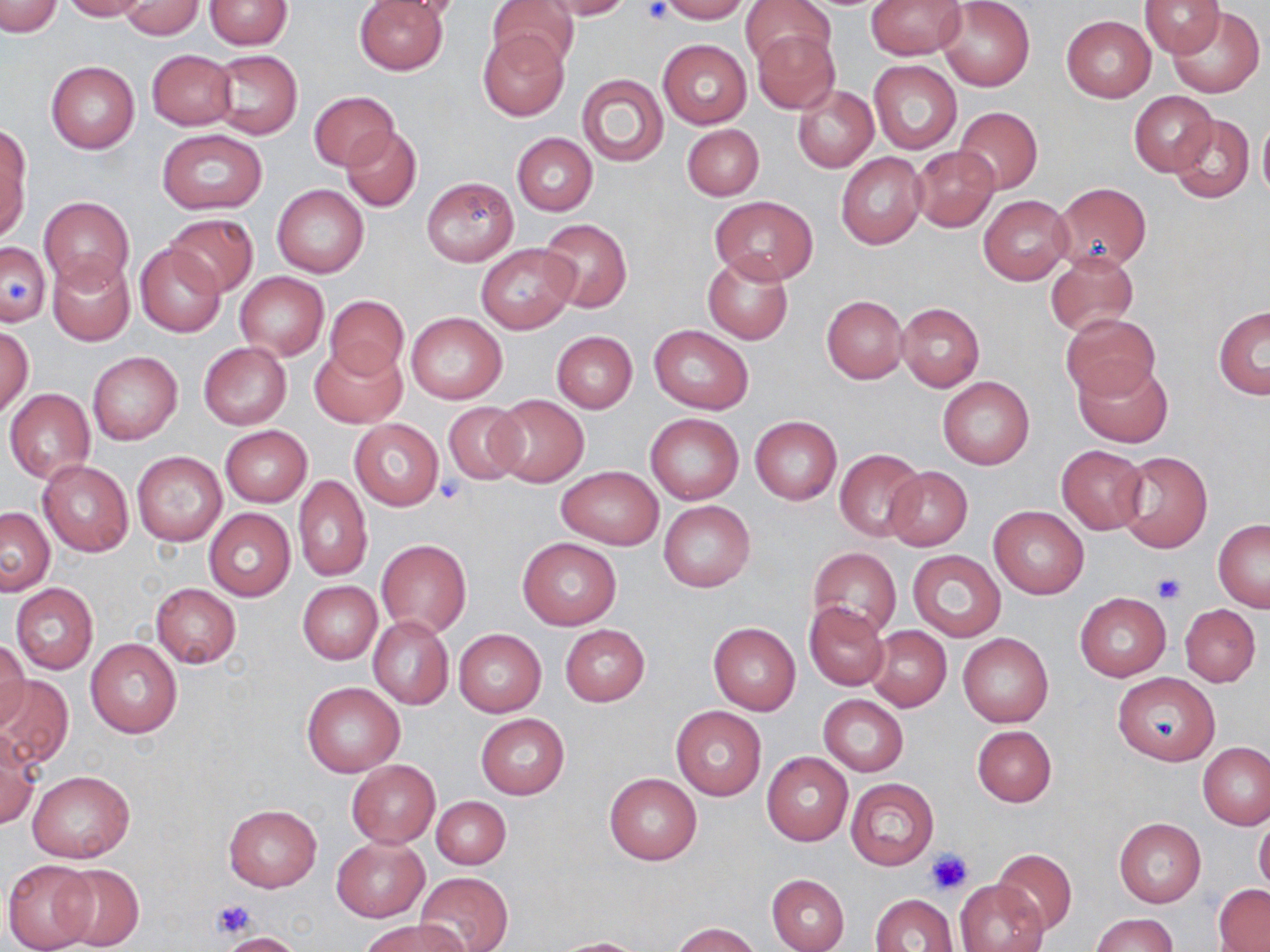
Approximate bounding boxes as [x1, y1, x2, y2] in pixels. Platelet locations: [637, 1, 671, 25], [7, 277, 33, 306], [434, 476, 465, 501], [1152, 573, 1187, 604], [927, 848, 974, 894], [211, 898, 253, 938]. Uninfected red blood cell locations: [1, 0, 61, 38], [60, 0, 150, 21], [204, 0, 292, 49], [353, 0, 447, 75], [377, 0, 469, 22], [487, 0, 579, 75], [541, 0, 632, 20], [659, 0, 749, 22], [741, 0, 835, 69], [866, 0, 962, 58], [1139, 0, 1226, 57], [937, 1, 1035, 90], [117, 2, 205, 39], [1166, 4, 1265, 98], [1060, 15, 1155, 102], [478, 30, 568, 120], [751, 30, 840, 114], [658, 39, 751, 127], [146, 49, 238, 131], [209, 49, 303, 139], [46, 60, 139, 153], [869, 60, 962, 155], [576, 73, 669, 167], [792, 85, 877, 172], [1129, 90, 1218, 175], [309, 91, 397, 171], [954, 106, 1042, 195], [1169, 114, 1254, 203], [1258, 115, 1270, 203], [682, 124, 764, 200], [339, 126, 422, 213], [0, 127, 30, 240], [156, 128, 267, 214], [512, 133, 598, 215], [911, 148, 999, 231], [836, 152, 927, 250], [421, 177, 518, 266], [1054, 182, 1151, 271], [272, 184, 369, 278], [38, 195, 134, 292], [978, 195, 1073, 284], [710, 196, 817, 283], [163, 214, 258, 297], [539, 218, 632, 312], [1, 239, 51, 328], [135, 242, 226, 337], [475, 244, 578, 332], [702, 251, 793, 345], [1044, 251, 1138, 338], [48, 255, 135, 347], [236, 272, 327, 358], [821, 294, 908, 383], [324, 295, 407, 381], [896, 303, 986, 391], [1213, 306, 1269, 399], [407, 312, 506, 404], [1061, 312, 1160, 402], [1, 325, 33, 418], [649, 325, 753, 414], [551, 331, 637, 413], [198, 342, 291, 429], [309, 344, 405, 427], [87, 351, 182, 445], [1074, 359, 1172, 447], [937, 376, 1035, 470], [5, 389, 96, 483], [488, 395, 589, 487], [442, 402, 526, 483], [646, 413, 743, 504], [749, 416, 841, 504], [349, 419, 443, 510], [219, 425, 312, 506], [1056, 445, 1147, 534], [833, 448, 925, 541], [131, 451, 227, 546], [1117, 451, 1213, 553], [39, 461, 134, 557], [883, 466, 972, 550], [556, 467, 664, 549], [292, 475, 373, 581], [658, 500, 756, 592], [988, 506, 1090, 599], [1, 507, 54, 595], [204, 509, 296, 601], [1213, 518, 1270, 611], [517, 537, 622, 629], [377, 539, 471, 638], [808, 547, 901, 639], [907, 550, 1006, 642], [298, 580, 382, 664], [10, 583, 98, 674], [151, 583, 241, 668], [1075, 593, 1171, 680], [804, 602, 890, 691], [1179, 604, 1262, 686], [368, 616, 454, 709], [708, 622, 801, 716], [866, 624, 951, 711], [560, 625, 649, 706], [454, 629, 546, 716], [958, 633, 1053, 728], [84, 638, 182, 737], [0, 640, 30, 729], [1114, 673, 1222, 765], [0, 674, 75, 770], [302, 682, 404, 776], [818, 694, 908, 777], [671, 706, 766, 800], [475, 713, 570, 799], [971, 725, 1056, 806], [0, 732, 39, 828], [1197, 743, 1270, 831], [761, 751, 854, 846], [347, 760, 440, 848], [29, 771, 134, 863], [605, 773, 701, 865], [846, 778, 939, 870], [433, 795, 511, 870], [224, 804, 321, 892], [1255, 817, 1270, 895], [1114, 818, 1206, 907], [330, 836, 428, 921], [994, 849, 1077, 934], [2, 858, 98, 952], [55, 863, 143, 951], [415, 871, 513, 952], [766, 874, 849, 952], [956, 879, 1048, 952], [1214, 886, 1270, 951], [871, 893, 958, 952], [1089, 913, 1179, 952], [361, 919, 466, 952], [672, 922, 762, 952], [218, 932, 306, 952], [550, 937, 648, 951]. Slide-level diagnosis: negative for blood parasites. Thin blood film. Image is 1270×952 pixels. Captured at 1000x magnification. Optical microscopy. Single field of view. May-Grünwald-Giemsa-stained preparation.